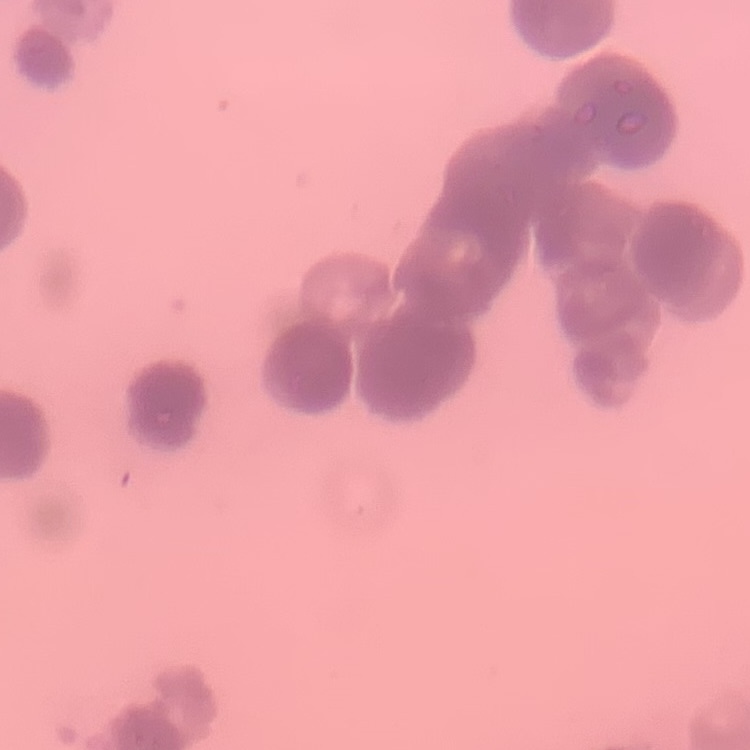 The red blood cells show rouleaux formation. Thin peripheral smear. Stained with either Field's or Giemsa. Square crop of a larger photomicrograph.